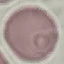
result = no malaria parasites seen
capture = smartphone camera at the microscope eyepiece
image type = cell patch, automatically extracted from a larger field of view and resized to 64 × 64 pixels
stain = Giemsa
preparation = thin blood film